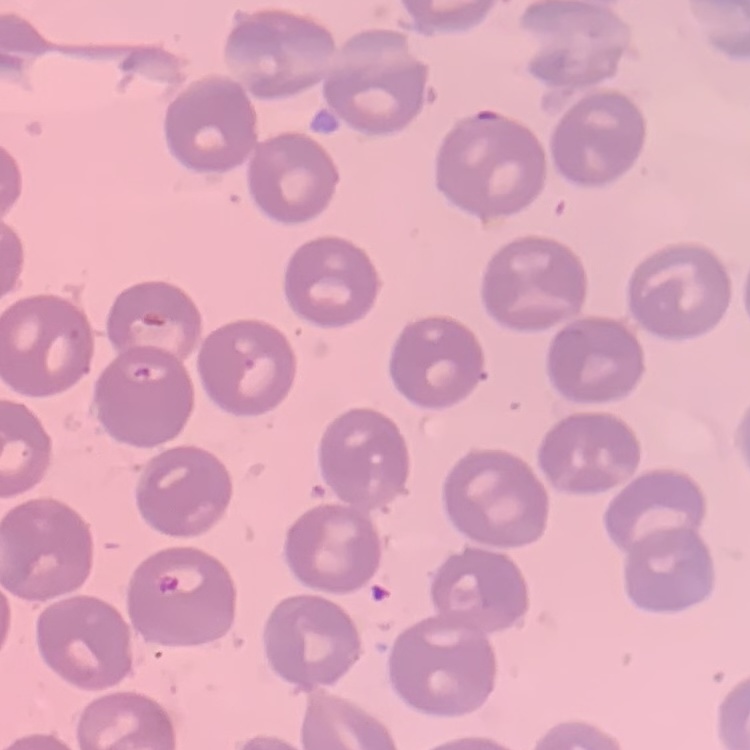
erythrocyte morphology = no rouleaux formation
stain = Field's or Giemsa
preparation = thin blood smear
image type = square crop of a larger photomicrograph